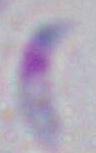
magnification = 1000x
modality = micrograph
identification = Toxoplasma gondii